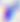
Summary:
  - Identification: Toxoplasma gondii
  - Modality: micrograph
  - Magnification: 400x